Report the malaria status of this cell.
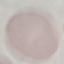

Uninfected.

stain = Giemsa
image type = automatically extracted cell patch, resized to 64 × 64 pixels
preparation = thin blood smear
capture = smartphone camera at the microscope eyepiece